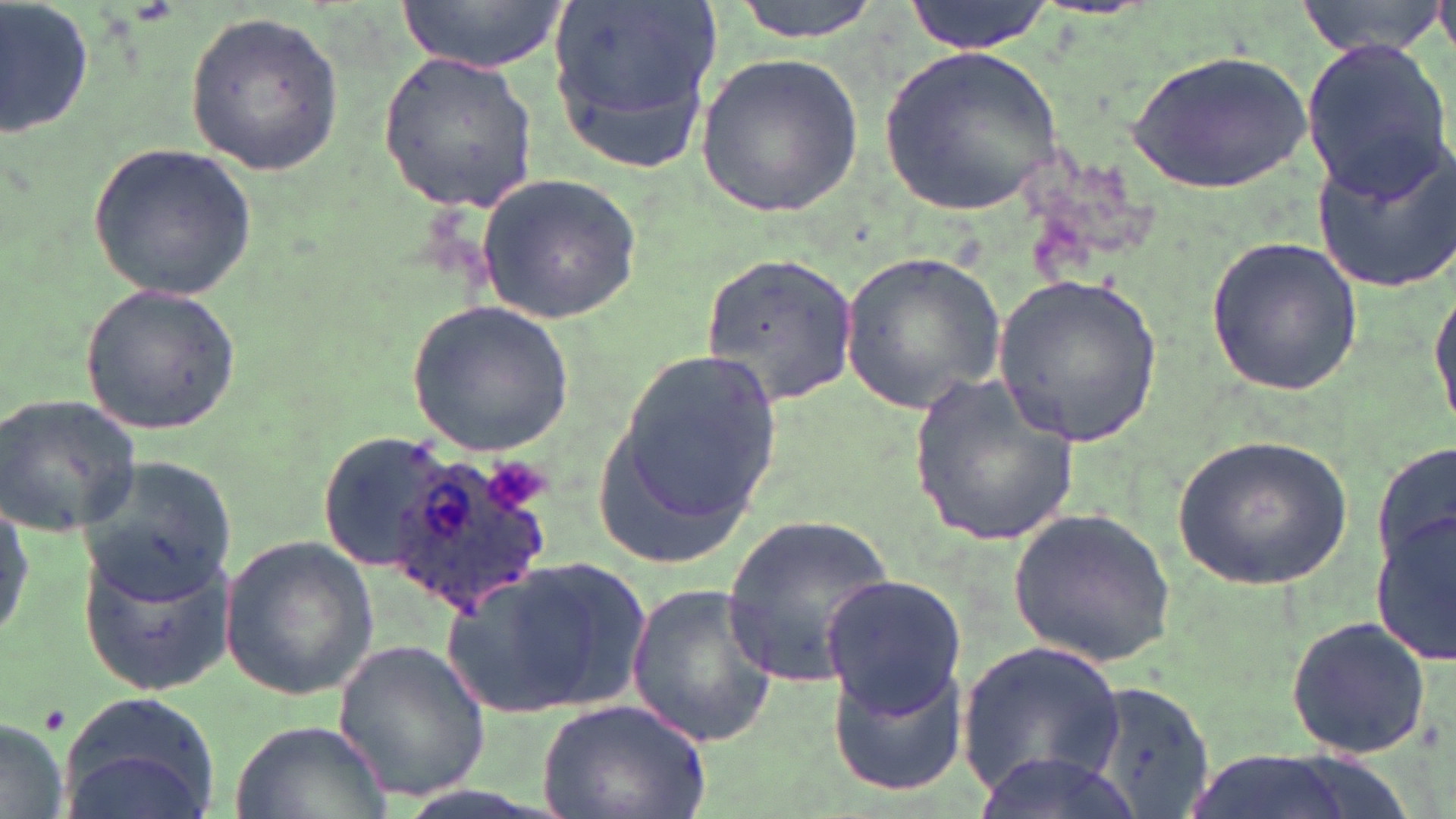
slide-level diagnosis = Plasmodium ovale
uninfected red blood cell locations = approximate bounding boxes as (x1,y1)-(x2,y2) corner pairs in pixels: (396,0)-(568,72), (547,0)-(720,171), (730,0)-(884,41), (904,0)-(1055,55), (1294,0)-(1450,58), (2,1)-(96,146), (184,11)-(343,174), (1300,40)-(1451,202), (882,48)-(1063,216), (1127,49)-(1313,192), (376,51)-(539,213), (695,52)-(864,218), (1310,137)-(1456,296), (85,139)-(263,302), (472,172)-(643,323), (1206,236)-(1363,396), (701,250)-(861,406), (840,250)-(1007,414), (1431,274)-(1456,434), (993,276)-(1167,446), (81,283)-(241,435), (406,300)-(574,455), (616,351)-(784,517), (907,372)-(1086,544), (0,390)-(144,539), (592,426)-(752,570), (1173,430)-(1356,589), (320,432)-(426,572), (1374,441)-(1454,574), (76,456)-(238,604), (1008,506)-(1177,666), (1372,508)-(1456,663), (723,515)-(896,689), (220,534)-(379,701), (75,535)-(239,691), (441,558)-(655,719), (822,575)-(966,715), (625,580)-(779,749), (1284,614)-(1434,762), (332,641)-(493,803), (960,641)-(1124,796), (829,658)-(970,795), (1086,678)-(1220,819), (52,690)-(222,819), (538,698)-(710,819), (0,718)-(72,816), (229,718)-(394,819), (1177,748)-(1370,819), (975,749)-(1147,819)
preparation = thin blood smear
magnification = 1000x
Plasmodium ovale-infected red blood cell locations = approximate bounding boxes as (x1,y1)-(x2,y2) corner pairs in pixels: (385,457)-(563,618)
modality = light microscopy
stain = May-Grünwald-Giemsa
image size = 1456×819 pixels
field of view = one of a larger specimen